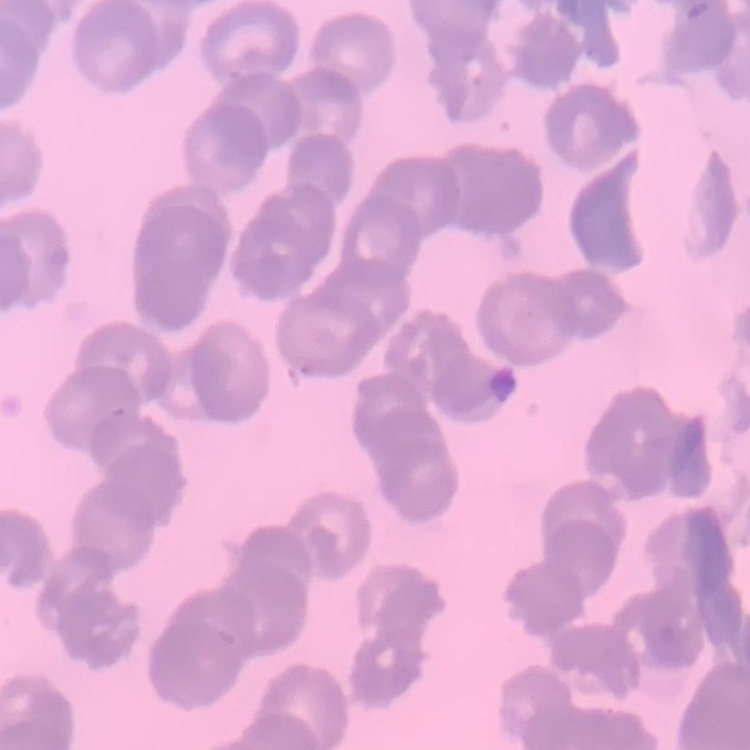
{
  "erythrocyte_morphology": "rouleaux formation",
  "stain": "Field's or Giemsa",
  "image_type": "square crop of a larger photomicrograph",
  "preparation": "thin blood smear"
}